State the blood parasite species.
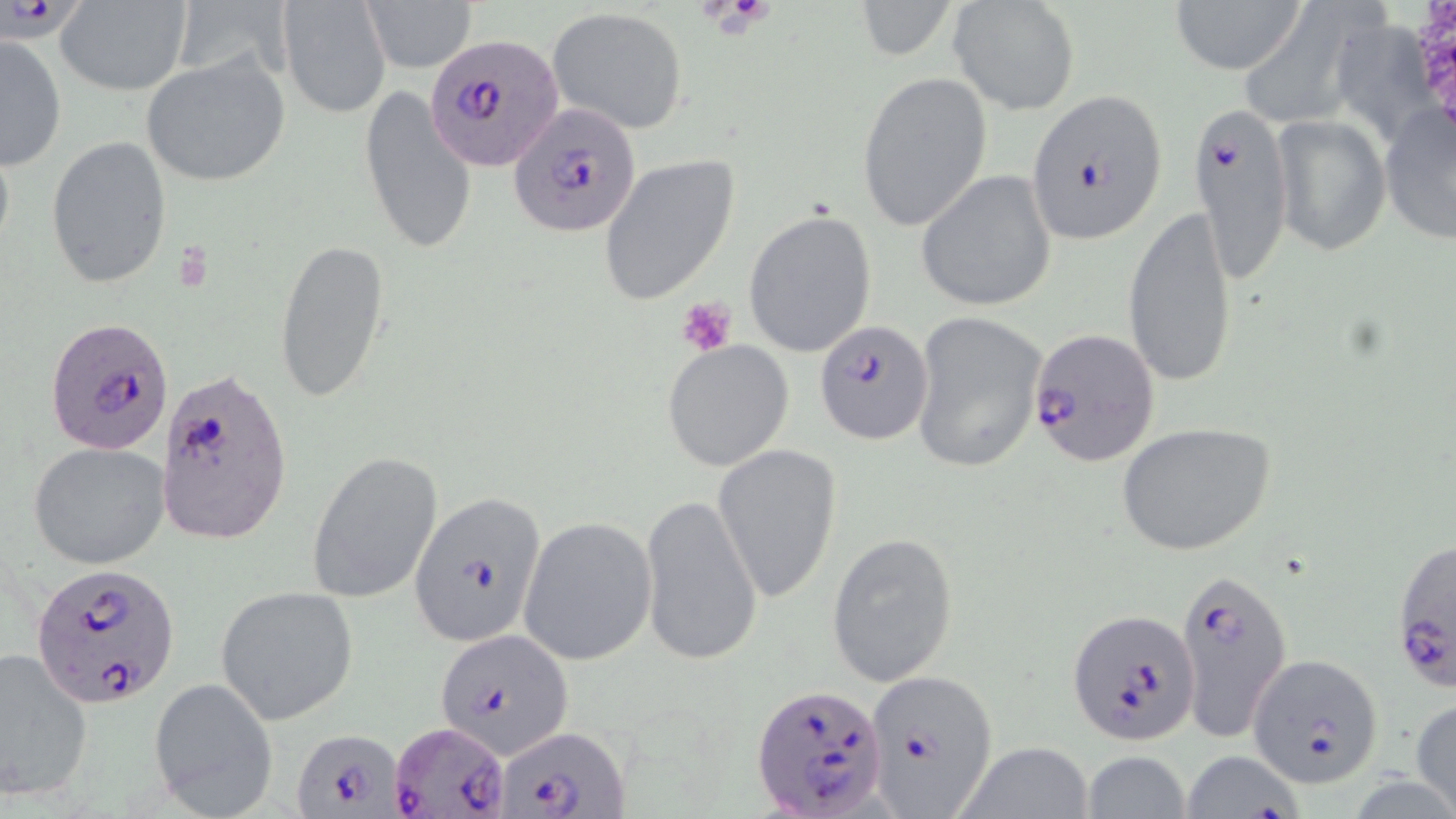
Plasmodium falciparum.

Summary:
  - Coordinate format: approximate bounding boxes as [x1, y1, x2, y2] in pixels
  - Platelet locations: [700, 0, 769, 37], [675, 296, 737, 357]
  - Uninfected red blood cell locations: [360, 0, 480, 74], [850, 0, 958, 66], [948, 0, 1080, 114], [1168, 0, 1306, 73], [1255, 0, 1400, 119], [55, 1, 192, 95], [279, 1, 389, 118], [546, 7, 691, 134], [1350, 23, 1445, 151], [1, 35, 68, 171], [142, 54, 289, 187], [855, 70, 992, 232], [358, 86, 477, 256], [1379, 94, 1455, 244], [1272, 114, 1390, 257], [46, 135, 173, 290], [598, 155, 740, 305], [916, 170, 1058, 312], [1122, 203, 1238, 391], [743, 208, 878, 360], [274, 236, 391, 406], [909, 311, 1048, 476], [662, 340, 795, 470], [1116, 422, 1275, 556], [28, 442, 170, 569], [712, 443, 844, 604], [306, 449, 443, 605], [640, 494, 762, 670], [518, 517, 656, 667], [827, 532, 959, 688], [215, 584, 360, 724], [0, 649, 96, 802], [147, 678, 278, 818], [1411, 696, 1456, 818], [951, 740, 1097, 819], [1179, 750, 1305, 819], [1081, 752, 1193, 817]
  - Plasmodium falciparum-infected red blood cell locations: [426, 35, 564, 171], [1027, 90, 1168, 243], [509, 102, 641, 238], [1190, 102, 1293, 284], [46, 315, 175, 455], [814, 321, 934, 445], [1027, 328, 1162, 470], [155, 366, 290, 547], [410, 490, 548, 648], [1388, 536, 1454, 695], [31, 564, 181, 707], [1173, 565, 1292, 744], [1068, 608, 1201, 747], [435, 630, 570, 755], [1247, 654, 1384, 790], [865, 670, 996, 815], [751, 685, 886, 818], [390, 720, 510, 816], [497, 726, 628, 818], [292, 728, 400, 817]
  - Magnification: 1000x
  - Image size: 1456×819 pixels
  - Stain: May-Grünwald-Giemsa
  - Field of view: one of a larger specimen
  - Modality: light microscopy
  - Preparation: thin blood smear